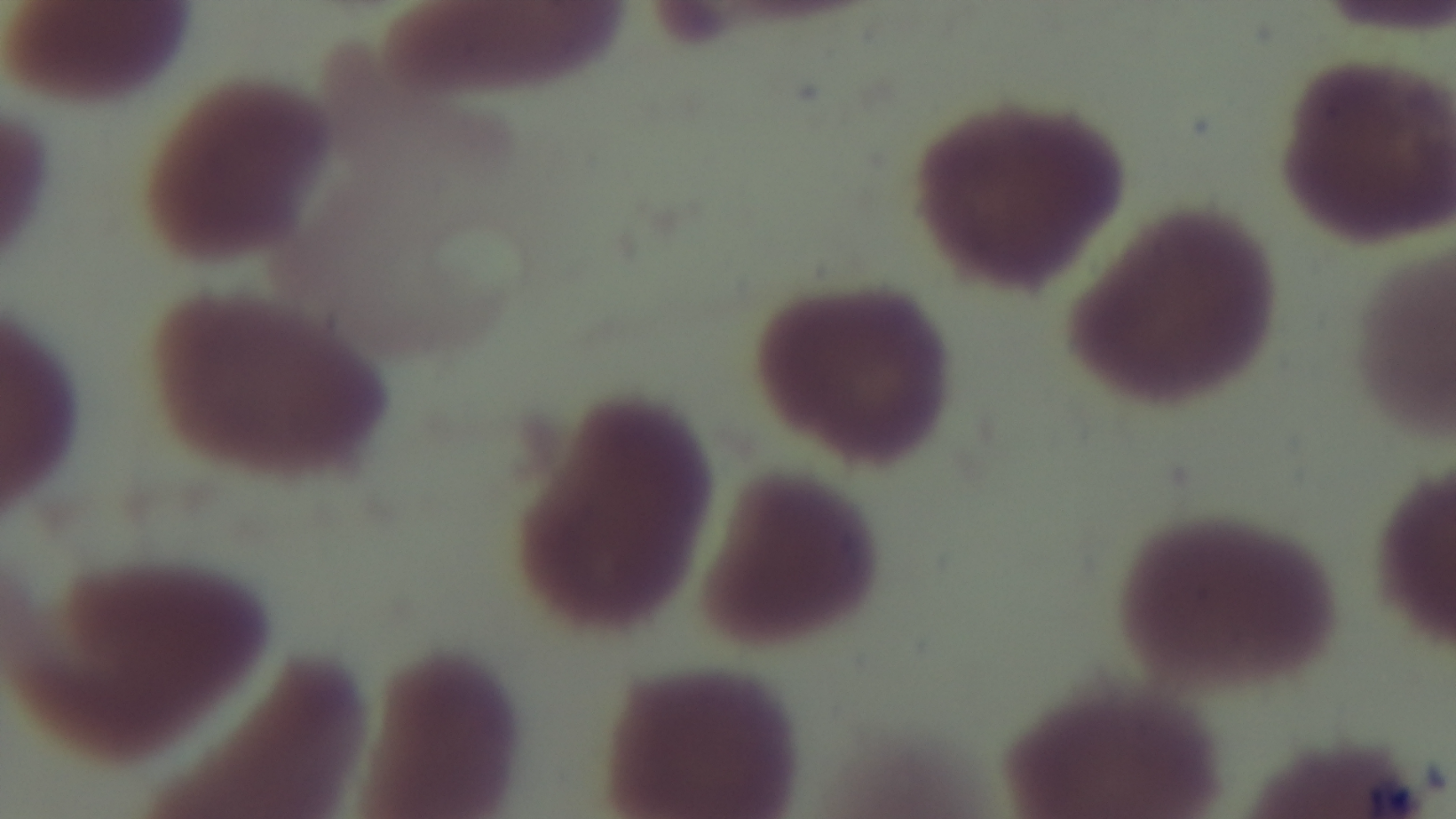 One field from the slide. Giemsa stain. 100x oil-immersion objective. Malaria status: negative. Preparation: thin blood film. Captured with a mounted 4K digital camera. Photomicrograph.